Comment on the morphology of the erythrocytes.
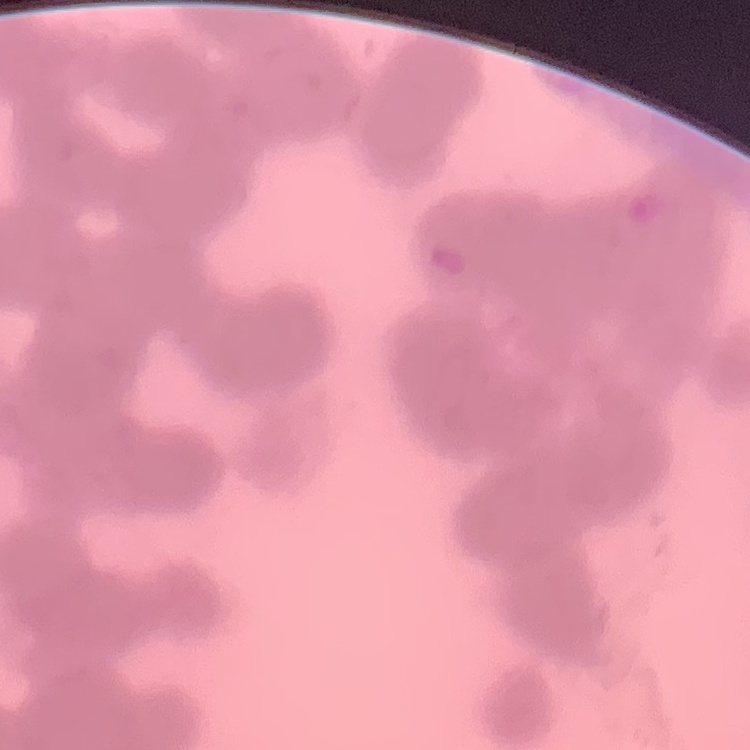
Rouleaux formation.

stain = Field's or Giemsa
preparation = thin peripheral smear
image type = square crop of a larger photomicrograph